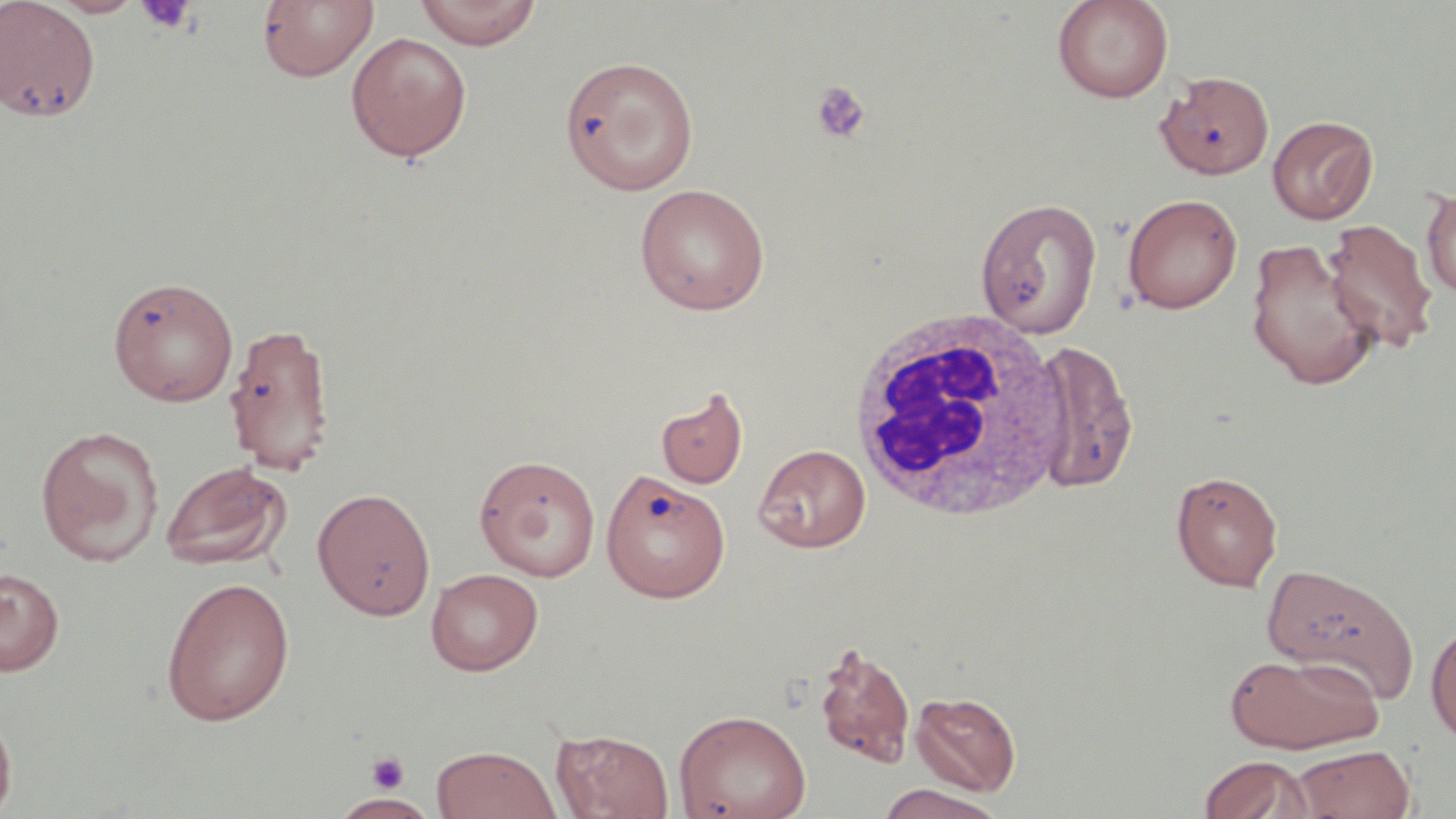

Approximate bounding boxes as [x1, y1, x2, y2] in pixels. White blood cell locations: [842, 309, 1073, 522]. Platelet locations: [136, 1, 196, 34], [810, 81, 870, 143], [366, 752, 409, 794]. Uninfected red blood cell locations: [0, 0, 100, 123], [48, 0, 145, 17], [415, 0, 542, 50], [1052, 0, 1174, 103], [257, 1, 378, 83], [345, 31, 472, 163], [559, 56, 699, 195], [1156, 70, 1275, 179], [1267, 115, 1378, 224], [634, 183, 770, 316], [1421, 187, 1456, 298], [1122, 193, 1242, 313], [975, 197, 1102, 338], [1322, 218, 1439, 352], [1244, 237, 1379, 391], [107, 275, 238, 406], [223, 321, 339, 473], [1030, 339, 1139, 493], [655, 386, 748, 489], [35, 424, 165, 566], [753, 444, 870, 552], [473, 454, 601, 581], [160, 460, 293, 571], [601, 467, 730, 603], [1171, 470, 1283, 591], [312, 487, 436, 620], [1262, 561, 1420, 704], [0, 567, 64, 676], [426, 567, 543, 675], [160, 575, 296, 727], [1426, 622, 1456, 744], [812, 641, 916, 770], [1224, 650, 1384, 754], [911, 691, 1021, 796], [0, 705, 17, 817], [674, 709, 812, 819], [551, 729, 674, 818], [431, 744, 560, 819], [1290, 745, 1416, 818], [1198, 755, 1311, 819], [877, 784, 1005, 819], [330, 794, 437, 817]. Slide-level diagnosis: negative for blood parasites. Thin blood smear. Image is 1456×819 pixels. May-Grünwald-Giemsa stain. Captured at 1000x magnification. One field of a larger specimen. Light microscopy.